Locate every blood parasite and identify its species.
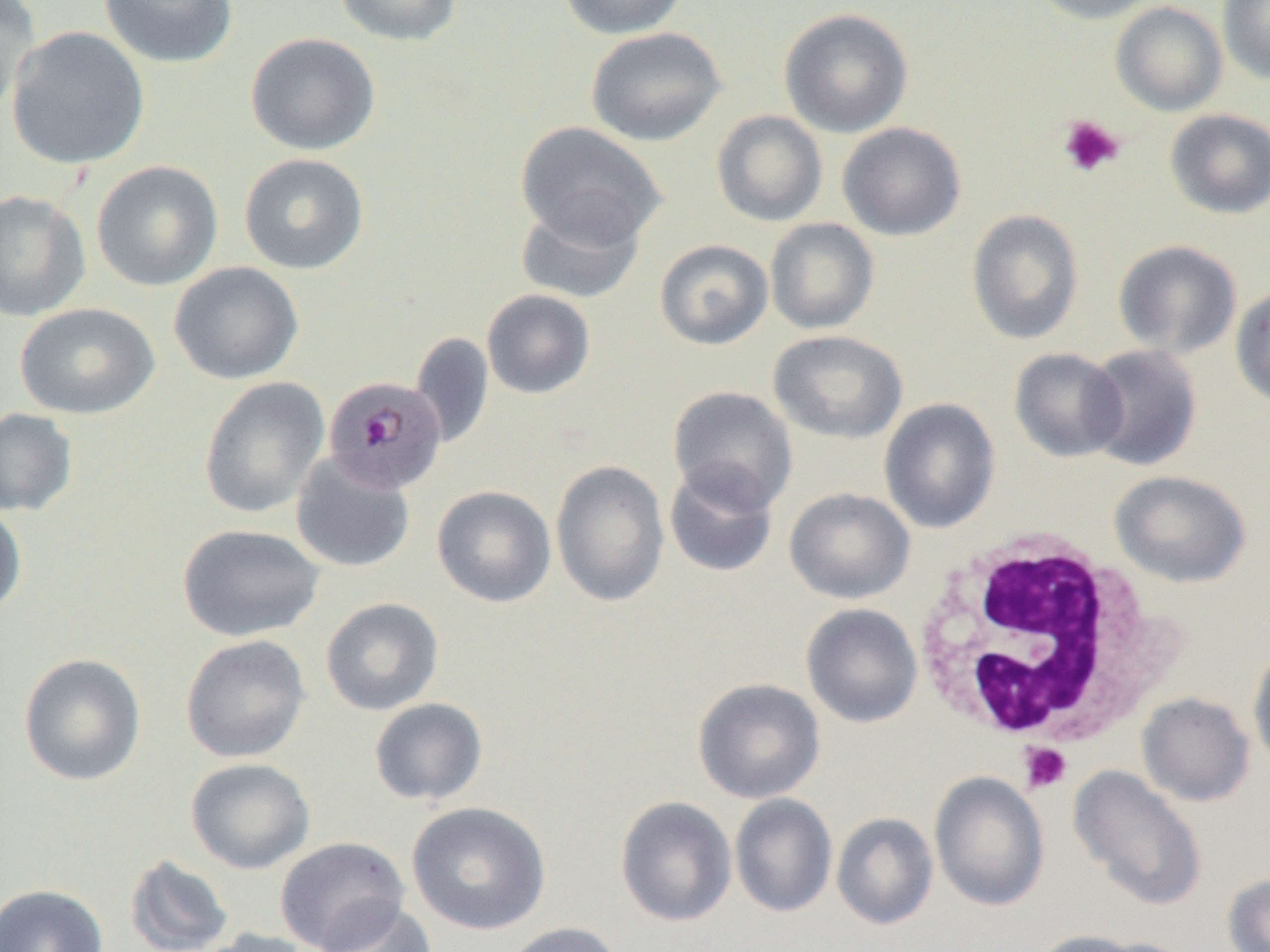
Approximate bounding boxes as [x1, y1, x2, y2] in pixels.
Plasmodium malariae-infected red blood cells: [323, 375, 450, 494].
No Plasmodium falciparum, Plasmodium ovale, Plasmodium vivax, Babesia divergens, or Trypanosoma brucei observed.

Uninfected red blood cell locations: [1, 0, 40, 118], [98, 0, 239, 69], [333, 0, 464, 46], [557, 0, 689, 40], [1030, 0, 1164, 24], [1217, 0, 1270, 84], [1111, 1, 1228, 116], [779, 8, 913, 138], [6, 26, 149, 170], [586, 27, 727, 146], [245, 32, 380, 156], [1165, 108, 1270, 219], [711, 110, 828, 227], [516, 121, 665, 249], [837, 122, 966, 241], [238, 152, 370, 275], [91, 160, 223, 292], [0, 190, 91, 322], [515, 199, 645, 303], [966, 209, 1084, 345], [764, 217, 880, 334], [654, 239, 774, 350], [1113, 240, 1242, 358], [168, 261, 304, 385], [1230, 284, 1270, 407], [482, 289, 595, 399], [14, 302, 159, 419], [768, 330, 908, 444], [410, 332, 494, 448], [1083, 344, 1202, 471], [1008, 347, 1128, 462], [198, 376, 330, 518], [667, 385, 798, 512], [879, 398, 1001, 534], [0, 407, 78, 517], [290, 452, 416, 573], [550, 459, 670, 608], [664, 461, 779, 579], [1109, 469, 1251, 588], [432, 485, 557, 608], [784, 487, 915, 604], [0, 501, 28, 620], [177, 523, 325, 642], [320, 597, 444, 715], [801, 603, 923, 728], [180, 634, 311, 763], [1248, 645, 1270, 770], [18, 652, 147, 786], [692, 677, 826, 803], [1137, 692, 1255, 807], [369, 697, 488, 806], [185, 757, 315, 874], [1067, 765, 1209, 912], [929, 772, 1050, 911], [729, 793, 837, 918], [615, 796, 737, 927], [406, 800, 551, 935], [831, 812, 939, 930], [275, 837, 410, 950], [125, 854, 234, 952], [1222, 872, 1270, 952], [0, 883, 108, 952], [316, 900, 438, 952], [498, 921, 627, 952], [193, 927, 319, 952], [1027, 930, 1147, 952]. White blood cell locations: [915, 531, 1179, 754]. Platelet locations: [1057, 114, 1125, 178], [1018, 742, 1072, 794]. Slide-level diagnosis: Plasmodium malariae. Captured at 1000x magnification. Thin blood film. Image is 1270×952 pixels. Light microscopy. Single field of view.